State which cell type is depicted.
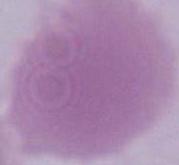

This is an erythrocyte.

Summary:
  - Modality: micrograph
  - Magnification: 1000x